Classify this cell by malaria status.
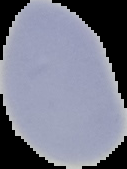

It is uninfected.

preparation = thin blood film
image type = cell region segmented out of the field of view; surrounding area masked to black
image size = 127×169 pixels